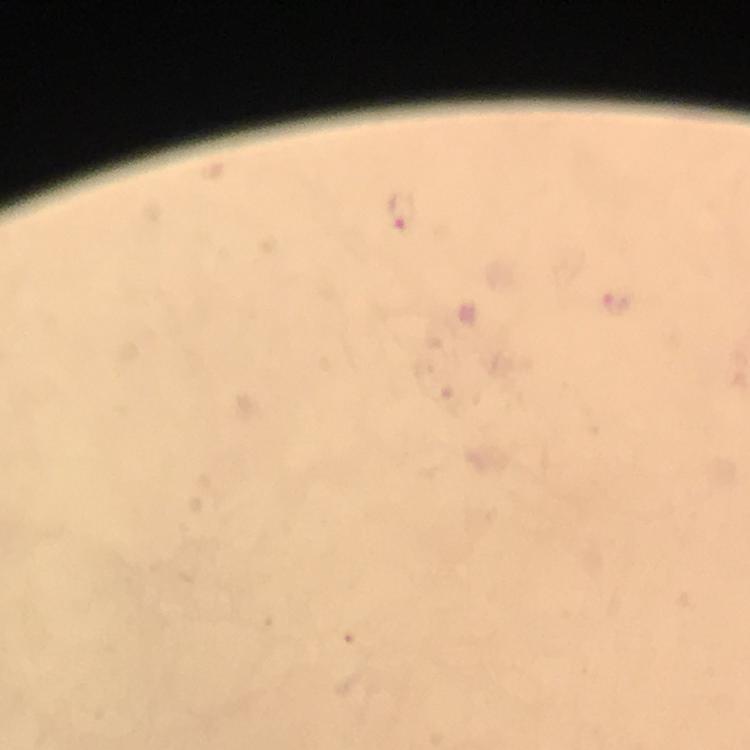

Approximate object centers, in pixels from the top-left corner. Plasmodium parasite locations: (x=400, y=209), (x=617, y=302). A crop from one field of view. At 100x magnification. Image is 750×750 pixels. Photographed through the microscope with a smartphone camera. Giemsa stain. Immersion oil was used. Thick blood film. From a malaria diagnostic workup.